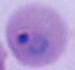
Summary:
  - Modality: micrograph
  - Magnification: 400x or 1000x
  - Identification: Plasmodium